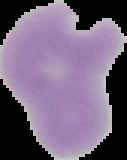 Image is 127×160 pixels. From a thin blood film. The area outside the segmented cell region is set to black. Result: no Plasmodium parasites seen.